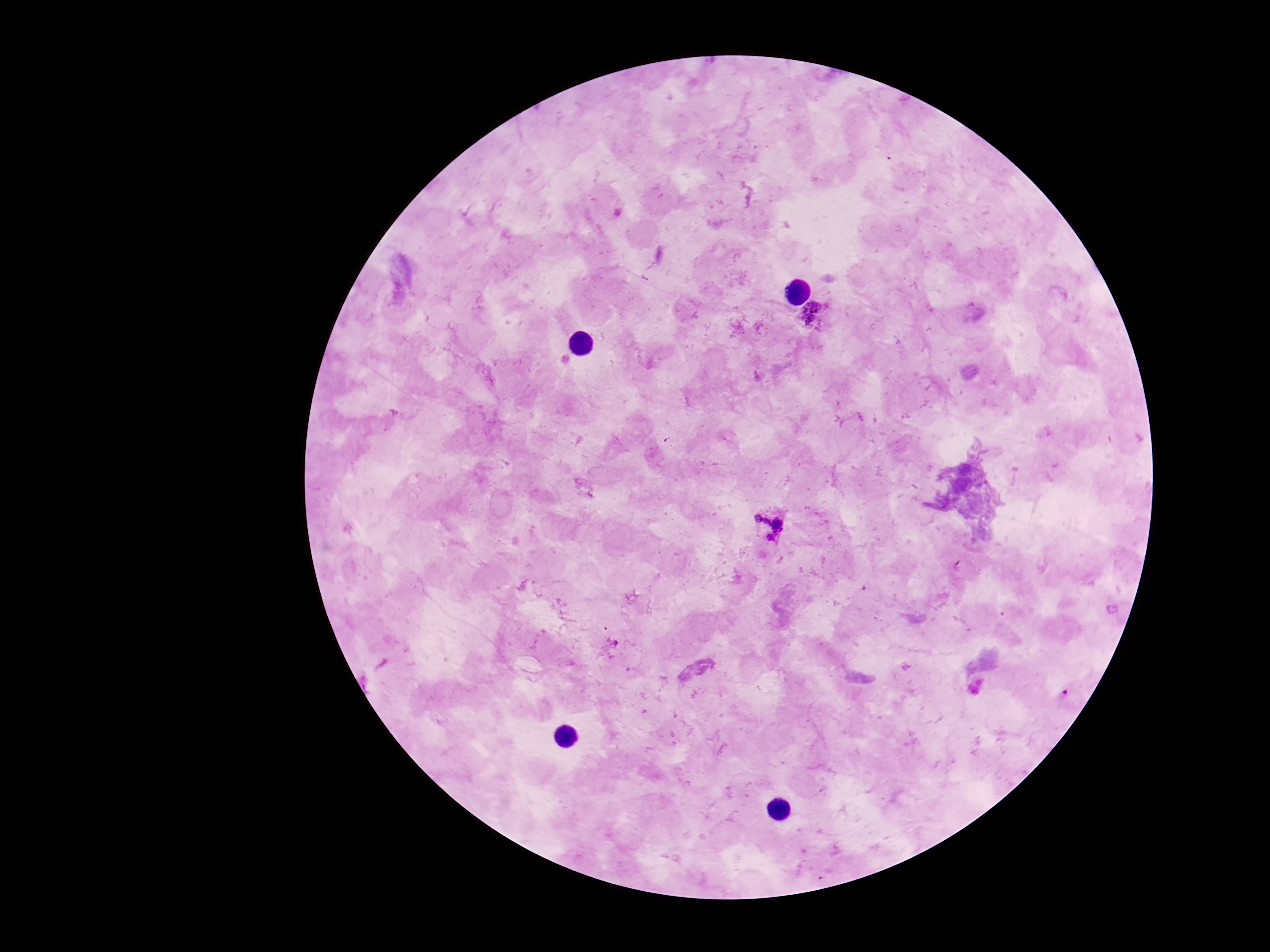

field_of_view: one from this slide
stain: Giemsa
plasmodium_parasite_locations: 'approximate object centers, in pixels from the top-left corner: (x=816, y=315), (x=771, y=524)'
magnification: 100x
capture: smartphone camera through the microscope eyepiece
preparation: thick blood smear
patient_malaria_status: infected
image_size: 1270×952 pixels